Outline each blood parasite and name the species.
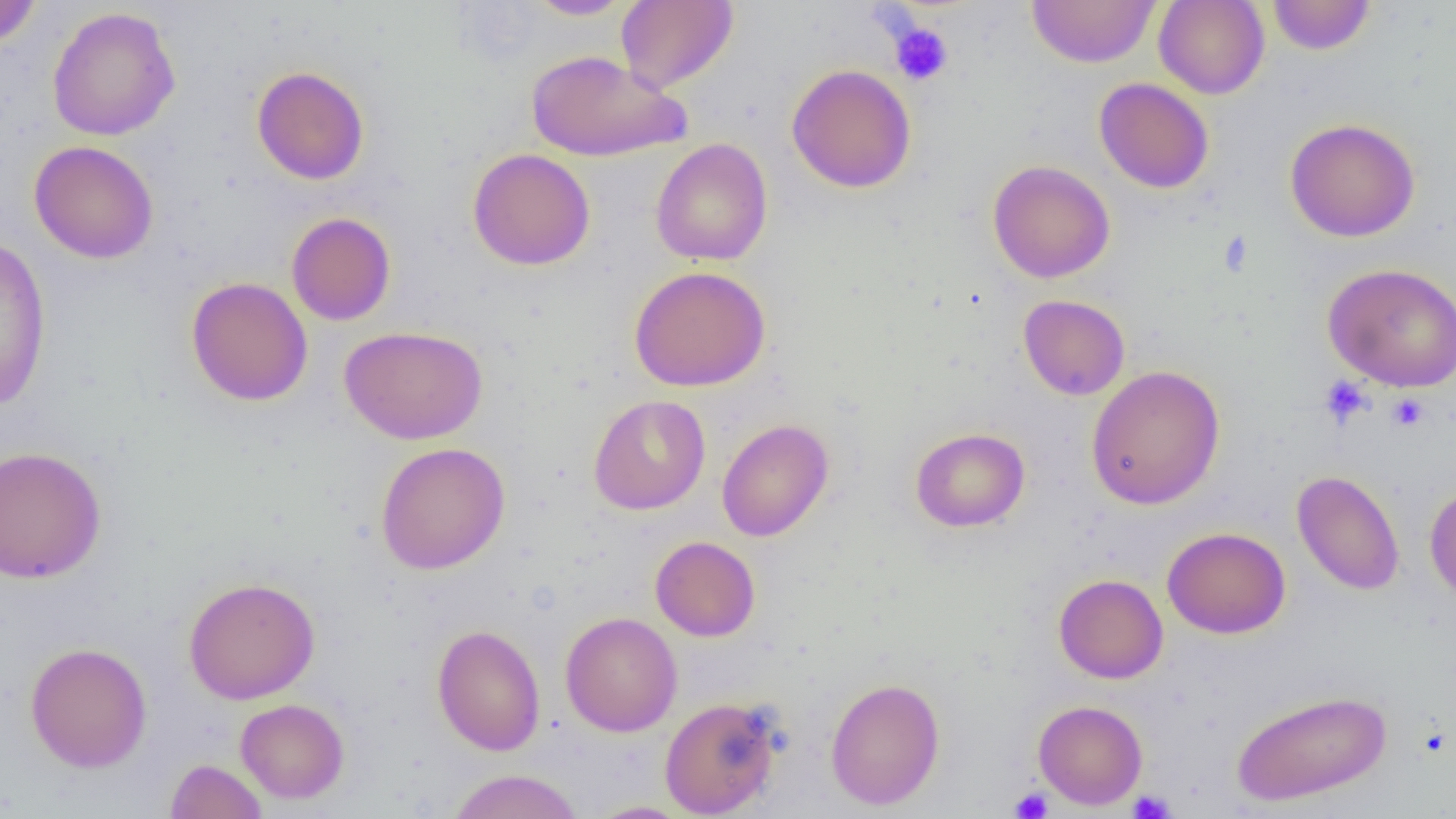

No blood parasites seen.

Summary:
  - Coordinate format: approximate bounding boxes as named x1/y1/x2/y2 corners in pixels
  - Uninfected red blood cell locations: (x1=0, y1=0, x2=43, y2=48), (x1=524, y1=0, x2=633, y2=20), (x1=616, y1=0, x2=739, y2=93), (x1=1027, y1=0, x2=1160, y2=68), (x1=1153, y1=0, x2=1270, y2=99), (x1=1267, y1=0, x2=1376, y2=55), (x1=46, y1=7, x2=181, y2=141), (x1=526, y1=49, x2=688, y2=162), (x1=787, y1=64, x2=917, y2=193), (x1=252, y1=66, x2=369, y2=185), (x1=1094, y1=77, x2=1214, y2=193), (x1=1284, y1=118, x2=1421, y2=242), (x1=650, y1=138, x2=772, y2=266), (x1=29, y1=140, x2=158, y2=264), (x1=468, y1=148, x2=595, y2=271), (x1=987, y1=160, x2=1115, y2=283), (x1=286, y1=212, x2=396, y2=326), (x1=0, y1=235, x2=52, y2=413), (x1=1322, y1=263, x2=1456, y2=391), (x1=629, y1=265, x2=770, y2=391), (x1=186, y1=277, x2=313, y2=406), (x1=1018, y1=294, x2=1130, y2=400), (x1=339, y1=325, x2=487, y2=445), (x1=1086, y1=365, x2=1225, y2=510), (x1=589, y1=395, x2=710, y2=515), (x1=717, y1=419, x2=834, y2=542), (x1=910, y1=427, x2=1029, y2=532), (x1=375, y1=442, x2=510, y2=575), (x1=0, y1=445, x2=106, y2=584), (x1=1292, y1=470, x2=1405, y2=595), (x1=1424, y1=484, x2=1456, y2=602), (x1=1162, y1=526, x2=1290, y2=639), (x1=650, y1=536, x2=761, y2=641), (x1=1053, y1=573, x2=1168, y2=684), (x1=183, y1=576, x2=320, y2=704), (x1=560, y1=611, x2=682, y2=737), (x1=431, y1=624, x2=545, y2=756), (x1=24, y1=642, x2=153, y2=772), (x1=825, y1=676, x2=945, y2=810), (x1=1230, y1=688, x2=1392, y2=808), (x1=659, y1=696, x2=783, y2=817), (x1=235, y1=698, x2=349, y2=803), (x1=1033, y1=699, x2=1147, y2=810), (x1=165, y1=758, x2=268, y2=819), (x1=446, y1=768, x2=584, y2=819), (x1=585, y1=800, x2=695, y2=818)
  - Platelet locations: (x1=889, y1=21, x2=953, y2=85), (x1=1319, y1=375, x2=1373, y2=428), (x1=1387, y1=393, x2=1430, y2=433), (x1=1010, y1=786, x2=1053, y2=818), (x1=1126, y1=789, x2=1176, y2=818)
  - Slide-level diagnosis: no evidence of blood parasites
  - Modality: optical microscopy
  - Field of view: one of a larger specimen
  - Magnification: 1000x
  - Preparation: thin blood smear
  - Image size: 1456×819 pixels